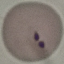 Result: malaria parasites detected. Giemsa stain. Thin smear of blood. Automatically extracted cell patch, resized to 64 × 64 pixels. Acquired by smartphone through the microscope eyepiece.